Give the extent of all Plasmodium ovale-infected red blood cells.
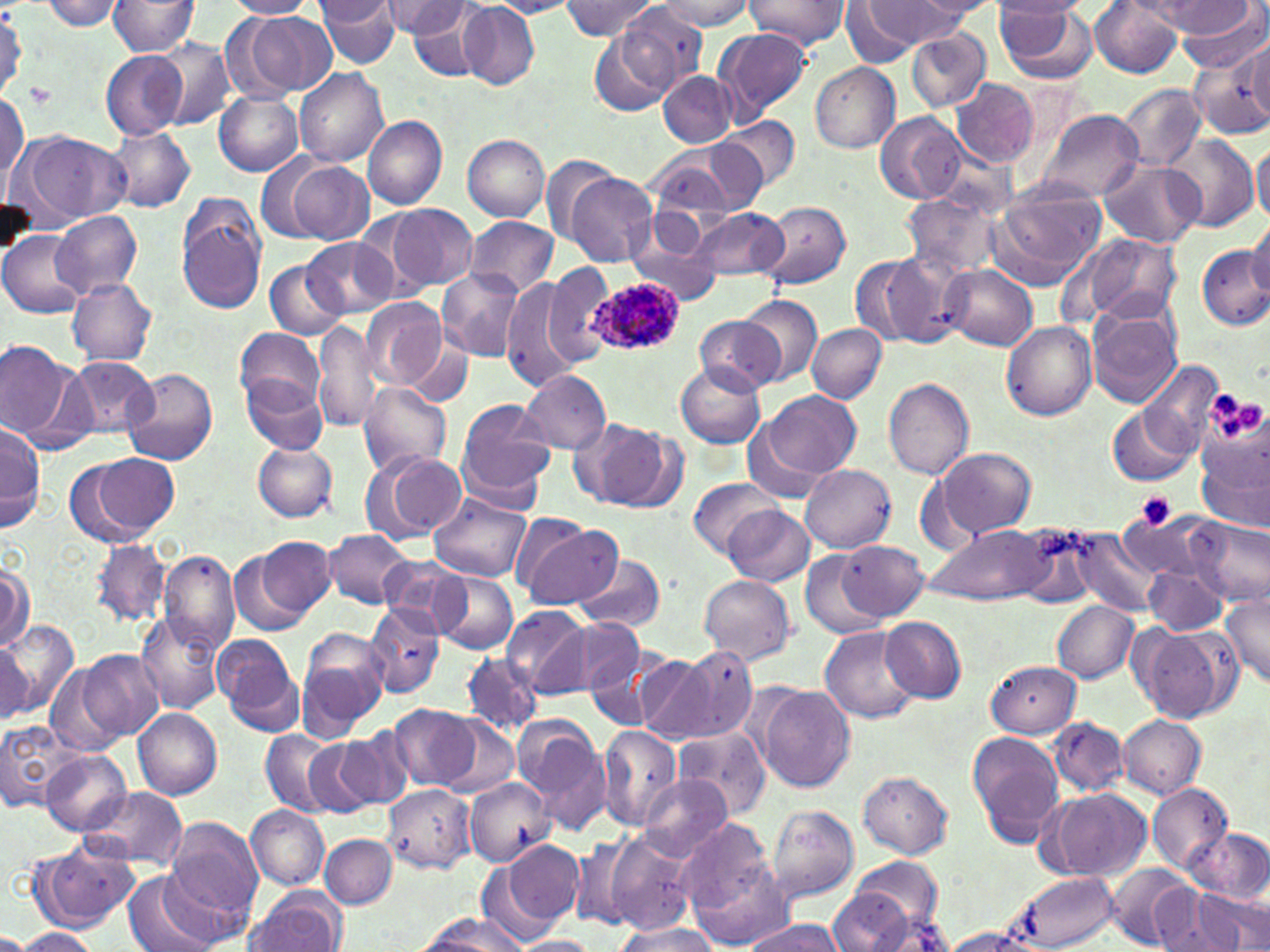
Approximate bounding boxes as [x1, y1, x2, y2] in pixels.
Plasmodium ovale-infected red blood cells: [584, 276, 684, 355].

Platelet locations: [25, 84, 56, 109], [1211, 390, 1239, 418], [1238, 399, 1265, 430], [1133, 492, 1177, 531]. Uninfected red blood cell locations: [40, 0, 126, 31], [226, 0, 316, 19], [316, 0, 401, 68], [561, 0, 661, 41], [746, 0, 850, 48], [905, 0, 996, 22], [994, 0, 1088, 19], [107, 1, 199, 57], [315, 1, 396, 29], [382, 1, 464, 40], [458, 1, 539, 90], [487, 1, 578, 17], [656, 1, 755, 31], [868, 1, 964, 46], [1090, 1, 1183, 77], [994, 2, 1084, 48], [1154, 2, 1256, 37], [1174, 2, 1269, 75], [842, 3, 919, 67], [407, 4, 491, 82], [997, 4, 1098, 85], [604, 7, 704, 108], [237, 11, 330, 99], [712, 27, 813, 124], [906, 29, 990, 113], [586, 34, 671, 116], [153, 37, 237, 131], [1246, 41, 1269, 124], [101, 50, 188, 140], [1189, 53, 1270, 139], [811, 62, 901, 153], [294, 68, 388, 167], [658, 71, 735, 147], [949, 78, 1038, 169], [1118, 85, 1206, 171], [0, 89, 28, 186], [213, 90, 303, 177], [1037, 109, 1143, 202], [874, 112, 969, 203], [363, 115, 447, 211], [724, 116, 800, 190], [106, 126, 196, 213], [16, 131, 128, 227], [463, 134, 549, 223], [1167, 135, 1259, 231], [1252, 142, 1270, 223], [673, 143, 766, 214], [256, 153, 334, 243], [540, 153, 618, 242], [1096, 158, 1208, 247], [651, 160, 736, 231], [282, 161, 376, 244], [566, 173, 658, 266], [988, 183, 1106, 287], [901, 191, 1004, 280], [175, 193, 269, 314], [757, 201, 851, 291], [387, 204, 477, 292], [688, 206, 790, 282], [51, 210, 142, 297], [465, 217, 559, 297], [1245, 219, 1270, 301], [624, 228, 722, 308], [0, 230, 89, 318], [1075, 234, 1182, 328], [305, 237, 395, 319], [1198, 246, 1270, 331], [883, 250, 972, 347], [850, 253, 937, 348], [265, 258, 348, 339], [542, 261, 618, 366], [943, 265, 1037, 351], [439, 268, 525, 361], [67, 277, 156, 365], [501, 280, 588, 393], [739, 294, 823, 386], [361, 297, 445, 388], [1087, 305, 1183, 408], [693, 314, 785, 395], [313, 320, 381, 434], [1001, 321, 1097, 421], [807, 323, 886, 403], [235, 327, 324, 410], [0, 339, 85, 450], [409, 341, 473, 403], [65, 357, 158, 439], [1141, 359, 1223, 454], [675, 363, 764, 449], [124, 369, 217, 466], [520, 370, 610, 454], [242, 373, 329, 453], [883, 379, 973, 481], [357, 381, 452, 477], [756, 391, 859, 480], [456, 400, 558, 506], [1106, 404, 1196, 486], [0, 424, 45, 534], [584, 424, 674, 510], [1197, 424, 1270, 538], [252, 441, 338, 522], [936, 447, 1035, 538], [79, 450, 179, 542], [368, 451, 466, 541], [800, 463, 895, 552], [689, 476, 782, 557], [429, 492, 533, 581], [724, 506, 814, 587], [710, 510, 813, 659], [1116, 510, 1219, 584], [1190, 514, 1269, 607], [516, 518, 619, 610], [1014, 522, 1102, 606], [926, 524, 1051, 605], [1070, 529, 1168, 619], [324, 530, 414, 610], [257, 536, 334, 618], [88, 538, 171, 629], [833, 542, 927, 621], [230, 546, 313, 637], [160, 548, 240, 653], [801, 550, 887, 637], [377, 556, 473, 634], [572, 557, 667, 631], [0, 562, 33, 654], [1142, 562, 1230, 637], [434, 572, 518, 655], [699, 575, 795, 665], [1220, 593, 1270, 688], [1053, 601, 1139, 683], [364, 602, 445, 697], [503, 605, 591, 697], [137, 612, 227, 715], [881, 618, 967, 702], [550, 619, 645, 698], [2, 621, 80, 718], [1131, 623, 1236, 725], [821, 626, 923, 723], [297, 631, 388, 739], [213, 633, 300, 731], [0, 638, 34, 720], [668, 647, 759, 744], [78, 649, 163, 742], [635, 651, 723, 745], [461, 653, 542, 736], [985, 660, 1081, 737], [45, 662, 129, 754], [756, 684, 855, 792], [388, 704, 481, 791], [134, 709, 223, 799], [1118, 714, 1207, 798], [439, 717, 519, 799], [1048, 718, 1129, 797], [0, 720, 81, 814], [597, 725, 682, 832], [519, 726, 613, 837], [674, 727, 770, 818], [259, 729, 343, 815], [336, 731, 412, 811], [968, 731, 1066, 844], [303, 740, 381, 816], [41, 751, 131, 836], [858, 771, 954, 859], [638, 773, 732, 861], [463, 779, 554, 867], [1147, 783, 1235, 875], [382, 785, 475, 872], [85, 787, 189, 874], [1044, 790, 1151, 881], [247, 805, 329, 890], [767, 805, 859, 904], [163, 816, 263, 925], [675, 824, 785, 943], [602, 826, 703, 932], [1186, 827, 1270, 902], [320, 834, 397, 908], [31, 838, 140, 933], [569, 839, 637, 930], [501, 840, 585, 930], [476, 854, 563, 949], [829, 863, 946, 949], [1105, 864, 1198, 948], [122, 870, 228, 952], [1004, 870, 1121, 952], [243, 888, 349, 952], [1150, 888, 1236, 952], [1192, 888, 1269, 948], [414, 913, 528, 951], [742, 917, 846, 952], [610, 921, 721, 951], [937, 927, 1046, 951], [12, 928, 100, 951], [512, 937, 599, 952]. Slide-level diagnosis: Plasmodium ovale. Single field of view. Image is 1270×952 pixels. May-Grünwald-Giemsa stain. Light microscopy. Captured at 1000x magnification. Thin blood smear.